Report the malaria status of this cell.
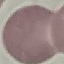

It is uninfected.

Acquired by smartphone through the microscope eyepiece. Giemsa stain. Cell patch, automatically extracted from a larger field of view and resized to 64 × 64 pixels. Thin blood film.